State the blood parasite species.
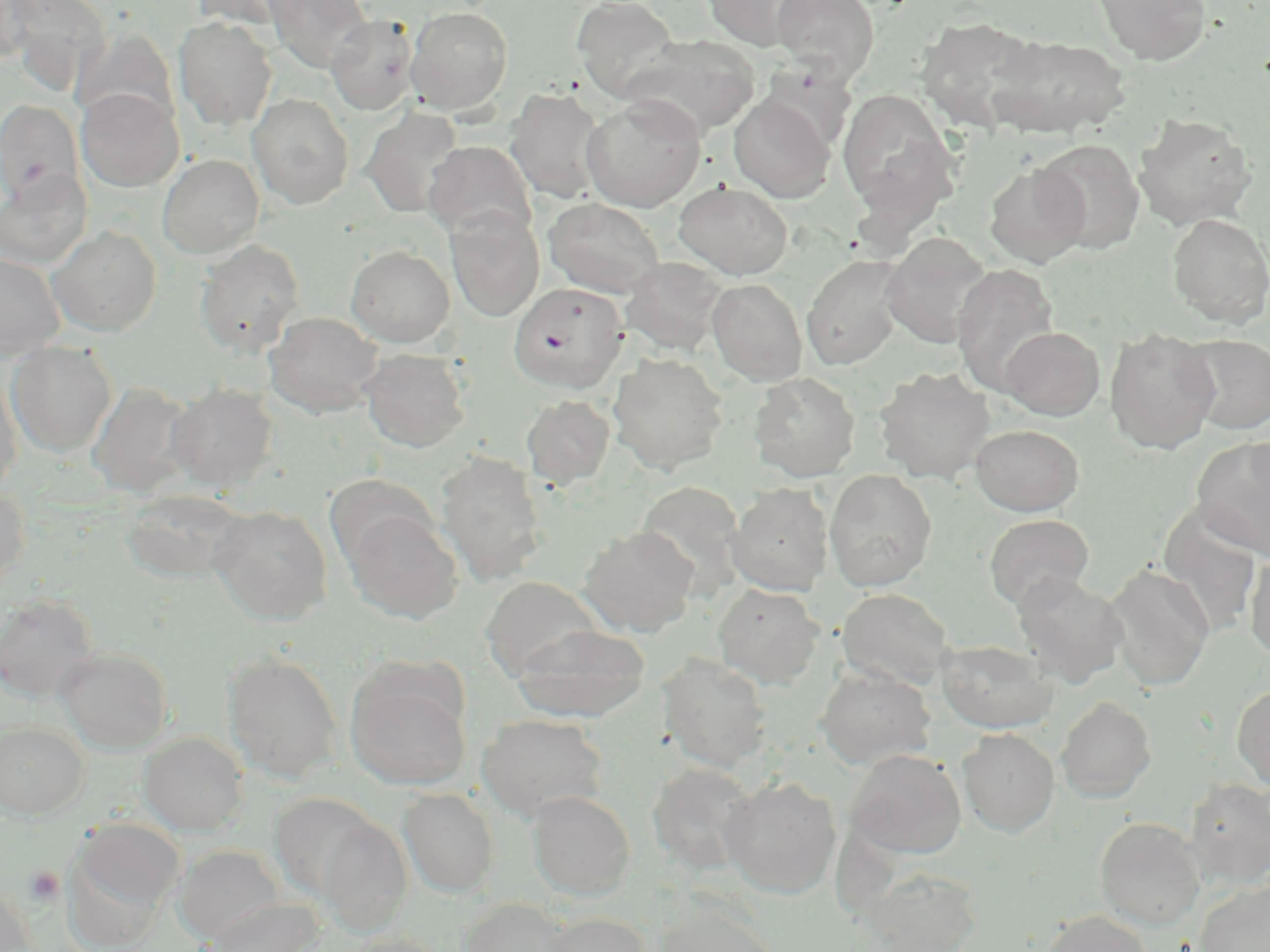
Plasmodium falciparum.

Approximate bounding boxes as (x1, y1, x2, y2) in pixels. Uninfected red blood cell locations: (1, 0, 35, 68), (3, 0, 110, 96), (188, 0, 302, 29), (265, 0, 373, 75), (572, 0, 683, 102), (703, 0, 815, 51), (771, 0, 878, 82), (1092, 0, 1212, 65), (405, 6, 513, 115), (326, 15, 418, 115), (914, 15, 1046, 133), (174, 17, 278, 130), (74, 28, 179, 131), (988, 34, 1131, 138), (622, 35, 760, 137), (757, 61, 858, 155), (76, 87, 184, 191), (505, 87, 609, 205), (837, 87, 960, 224), (247, 93, 354, 209), (581, 94, 706, 212), (728, 95, 835, 202), (0, 100, 84, 205), (361, 107, 464, 218), (1133, 113, 1257, 230), (1034, 139, 1145, 254), (424, 140, 537, 242), (157, 154, 264, 258), (984, 163, 1090, 267), (0, 169, 91, 269), (674, 181, 793, 279), (543, 197, 666, 298), (446, 208, 545, 322), (1166, 213, 1270, 328), (48, 227, 162, 336), (880, 233, 994, 349), (194, 240, 305, 357), (346, 245, 455, 346), (0, 253, 65, 358), (801, 255, 906, 370), (620, 257, 729, 356), (951, 262, 1060, 396), (707, 278, 808, 385), (265, 311, 383, 417), (1000, 326, 1105, 420), (1104, 327, 1221, 454), (1181, 334, 1270, 434), (7, 342, 117, 457), (359, 348, 470, 452), (608, 352, 728, 475), (874, 366, 995, 483), (0, 370, 23, 496), (750, 372, 860, 481), (87, 382, 199, 496), (166, 383, 279, 492), (522, 395, 615, 488), (970, 424, 1084, 516), (1192, 435, 1270, 560), (435, 451, 549, 586), (824, 470, 937, 590), (322, 474, 435, 567), (634, 480, 747, 599), (727, 483, 834, 596), (0, 484, 30, 596), (121, 490, 249, 584), (209, 505, 332, 624), (1157, 505, 1264, 636), (343, 508, 462, 623), (984, 514, 1094, 612), (579, 526, 699, 636), (1244, 551, 1270, 662), (1105, 563, 1214, 691), (1012, 571, 1129, 687), (480, 577, 604, 681), (713, 583, 825, 688), (836, 588, 956, 690), (0, 594, 100, 703), (511, 623, 651, 722), (937, 639, 1058, 733), (56, 646, 174, 753), (223, 651, 344, 784), (658, 654, 773, 771), (815, 665, 936, 769), (347, 669, 472, 790), (1232, 684, 1270, 791), (1056, 697, 1156, 802), (477, 713, 610, 821), (0, 721, 89, 819), (958, 727, 1059, 835), (139, 732, 248, 834), (845, 749, 966, 859), (647, 762, 759, 876), (721, 775, 841, 898), (1185, 778, 1270, 888), (398, 788, 500, 897), (527, 790, 636, 900), (269, 793, 382, 899), (1095, 817, 1206, 930), (73, 818, 184, 920), (317, 818, 412, 934), (174, 844, 286, 943), (860, 867, 983, 952), (1195, 880, 1270, 952), (0, 885, 37, 952), (205, 897, 322, 952), (459, 899, 575, 952), (652, 902, 780, 952), (1039, 910, 1156, 952), (540, 912, 652, 952), (342, 931, 448, 952). Plasmodium falciparum-infected red blood cell locations: (510, 282, 627, 392). Platelet locations: (25, 865, 65, 906). Captured at 1000x magnification. May-Grünwald-Giemsa-stained preparation. Image is 1270×952 pixels. Light microscopy. Thin blood film. One field of a larger specimen.